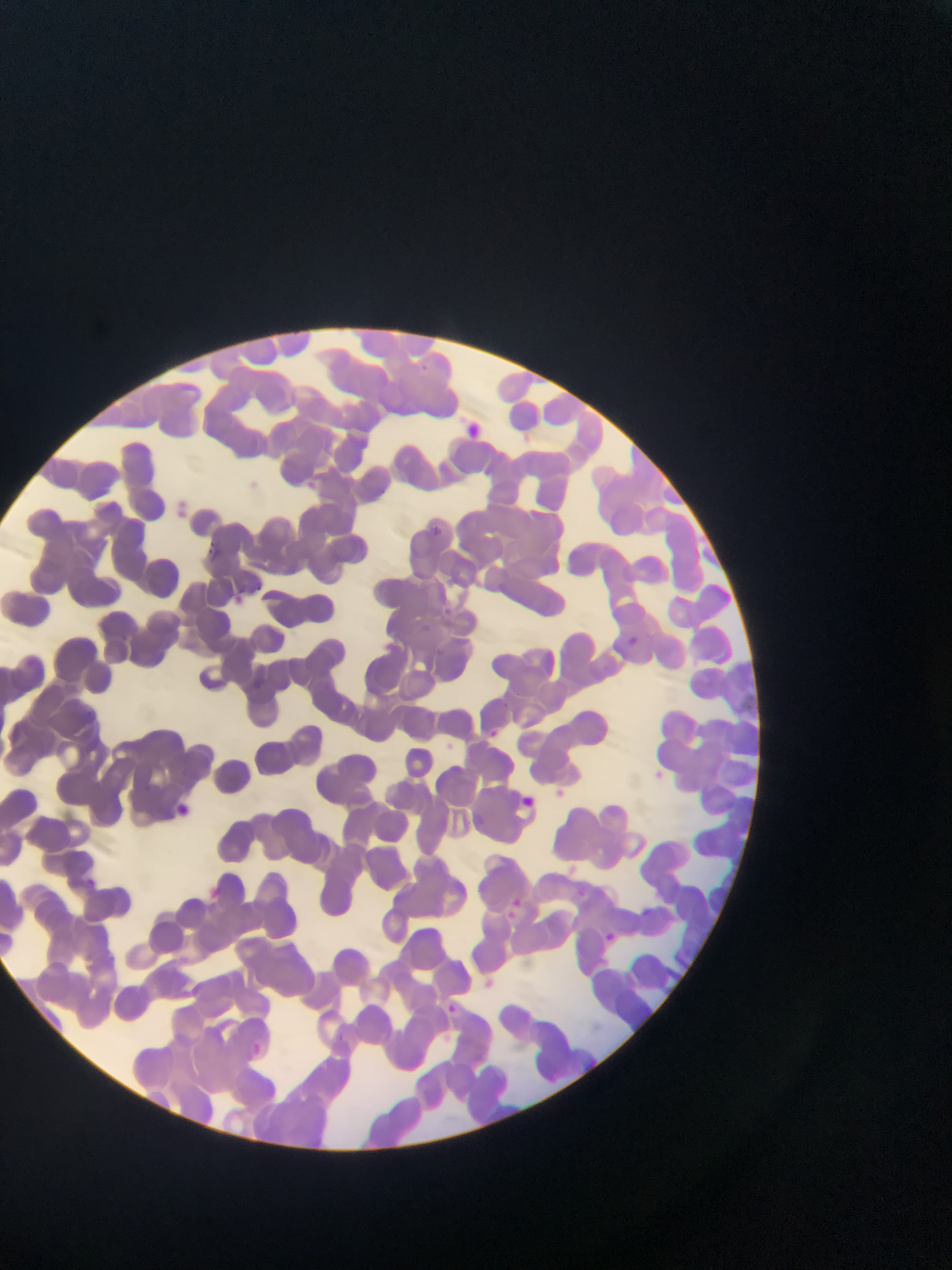

Approximate bounding boxes as (left, top, right, bottom) in pixels.
Summary:
  - Plasmodium parasite locations: (418, 357, 434, 374), (481, 459, 511, 487), (430, 525, 449, 549), (195, 533, 223, 559), (239, 586, 266, 612), (444, 607, 461, 623), (626, 638, 662, 662), (434, 646, 457, 666), (196, 676, 233, 698), (497, 695, 513, 707), (491, 731, 504, 744), (556, 786, 571, 798), (516, 788, 532, 817), (172, 802, 198, 826), (565, 861, 581, 874), (84, 876, 113, 898), (199, 877, 240, 920), (513, 894, 530, 907), (632, 901, 654, 915), (502, 908, 520, 924), (596, 925, 618, 952), (479, 974, 513, 1004), (444, 999, 477, 1031), (330, 1031, 363, 1056), (245, 1042, 273, 1070)
  - Field of view: single
  - Capture: mobile-phone photograph through a microscope
  - Country: Ghana
  - Preparation: thin blood film
  - Image size: 952×1270 pixels